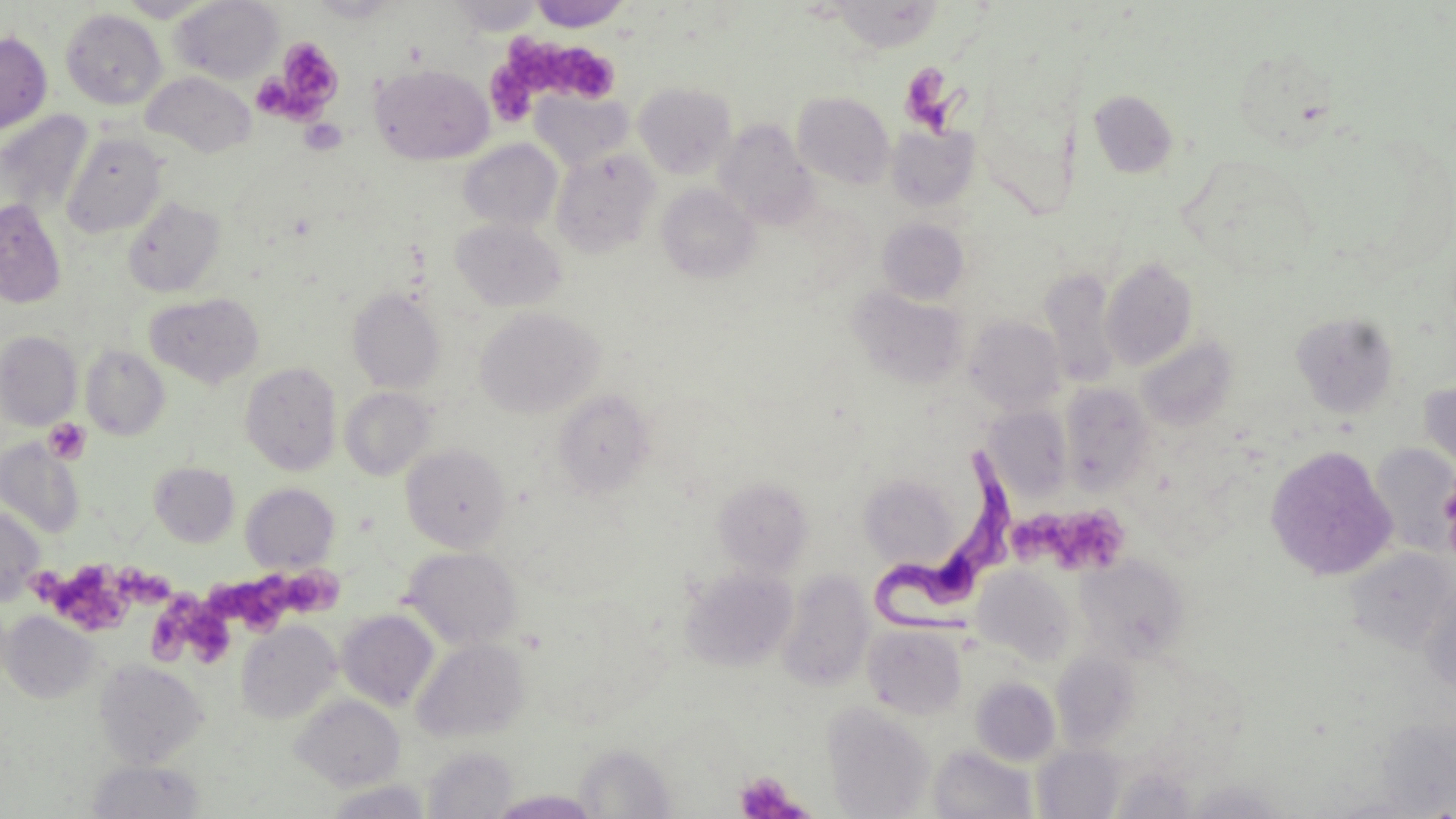

slide-level diagnosis = Trypanosoma brucei
uninfected red blood cell locations = approximate bounding boxes as (x1, y1, x2, y2) in pixels: (116, 0, 218, 22), (446, 0, 546, 36), (827, 0, 946, 53), (170, 1, 283, 84), (529, 1, 630, 31), (60, 8, 167, 110), (0, 31, 52, 134), (371, 64, 493, 165), (141, 71, 256, 157), (634, 82, 736, 179), (1088, 90, 1178, 178), (531, 91, 633, 171), (793, 91, 895, 189), (0, 111, 94, 221), (714, 119, 817, 227), (887, 124, 979, 211), (62, 134, 168, 237), (458, 139, 563, 233), (551, 148, 660, 257), (657, 184, 759, 283), (123, 196, 225, 297), (0, 199, 66, 307), (451, 218, 567, 312), (877, 218, 969, 304), (1102, 257, 1199, 370), (1041, 269, 1120, 388), (849, 287, 970, 390), (347, 288, 445, 394), (147, 292, 264, 388), (476, 307, 603, 418), (1291, 312, 1398, 416), (965, 316, 1066, 415), (0, 331, 81, 430), (1137, 336, 1236, 430), (81, 346, 170, 440), (240, 362, 342, 475), (1419, 379, 1456, 481), (1058, 382, 1154, 496), (340, 387, 435, 480), (552, 389, 656, 499), (985, 404, 1073, 502), (0, 440, 85, 539), (401, 443, 511, 552), (1370, 443, 1455, 554), (1265, 445, 1397, 581), (148, 462, 239, 547), (865, 466, 957, 573), (712, 476, 813, 578), (241, 483, 339, 572), (0, 507, 43, 605), (402, 546, 523, 650), (1344, 548, 1454, 654), (1076, 554, 1189, 663), (680, 566, 798, 672), (973, 566, 1078, 665), (777, 569, 874, 692), (1421, 581, 1456, 702), (337, 610, 439, 711), (2, 611, 100, 703), (235, 620, 342, 724), (862, 623, 969, 719), (411, 637, 531, 744), (1050, 649, 1142, 752), (94, 659, 207, 767), (970, 677, 1061, 766), (290, 695, 405, 791), (823, 703, 935, 819), (574, 743, 678, 818), (928, 744, 1038, 819), (1034, 745, 1125, 818), (422, 746, 516, 818), (87, 759, 206, 818), (1184, 779, 1290, 818), (323, 780, 433, 819), (490, 789, 600, 818), (1323, 794, 1443, 818)
Trypanosoma brucei locations = approximate bounding boxes as (x1, y1, x2, y2) in pixels: (869, 446, 1018, 637)
stain = May-Grünwald-Giemsa
magnification = 1000x
field of view = one of a larger specimen
modality = optical microscopy
platelet locations = approximate bounding boxes as (x1, y1, x2, y2) in pixels: (274, 36, 344, 116), (508, 37, 623, 103), (902, 59, 969, 136), (489, 62, 535, 124), (300, 118, 347, 155), (45, 418, 91, 464), (1012, 505, 1077, 569), (1055, 507, 1133, 577), (35, 560, 133, 629), (123, 562, 178, 611), (220, 566, 291, 635), (283, 572, 350, 617), (153, 592, 232, 662), (734, 770, 807, 818)
preparation = thin blood film
image size = 1456×819 pixels